Assess this cell for malaria.
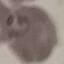
Parasitized.

{
  "stain": "Giemsa",
  "image_type": "cell patch, automatically extracted from a larger field of view and resized to 64 × 64 pixels",
  "capture": "smartphone camera at the microscope eyepiece",
  "preparation": "thin blood smear"
}